State which parasite is depicted.
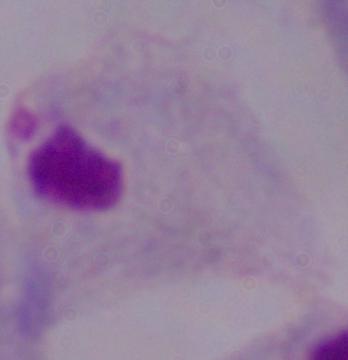

A trichomonad.

Photomicrograph. 1000x magnification.